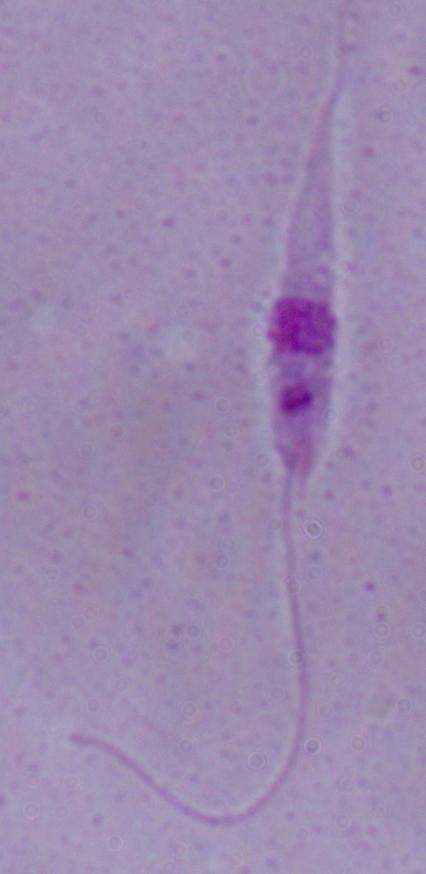
modality = micrograph
identification = Leishmania
magnification = 1000x